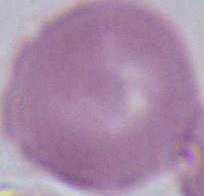

Summary:
  - Identification: red blood cell
  - Modality: photomicrograph
  - Magnification: 1000x